Identify the parasite.
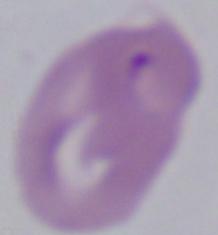

Babesia.

1000x magnification. Photomicrograph.